Look for parasitized red blood cells.
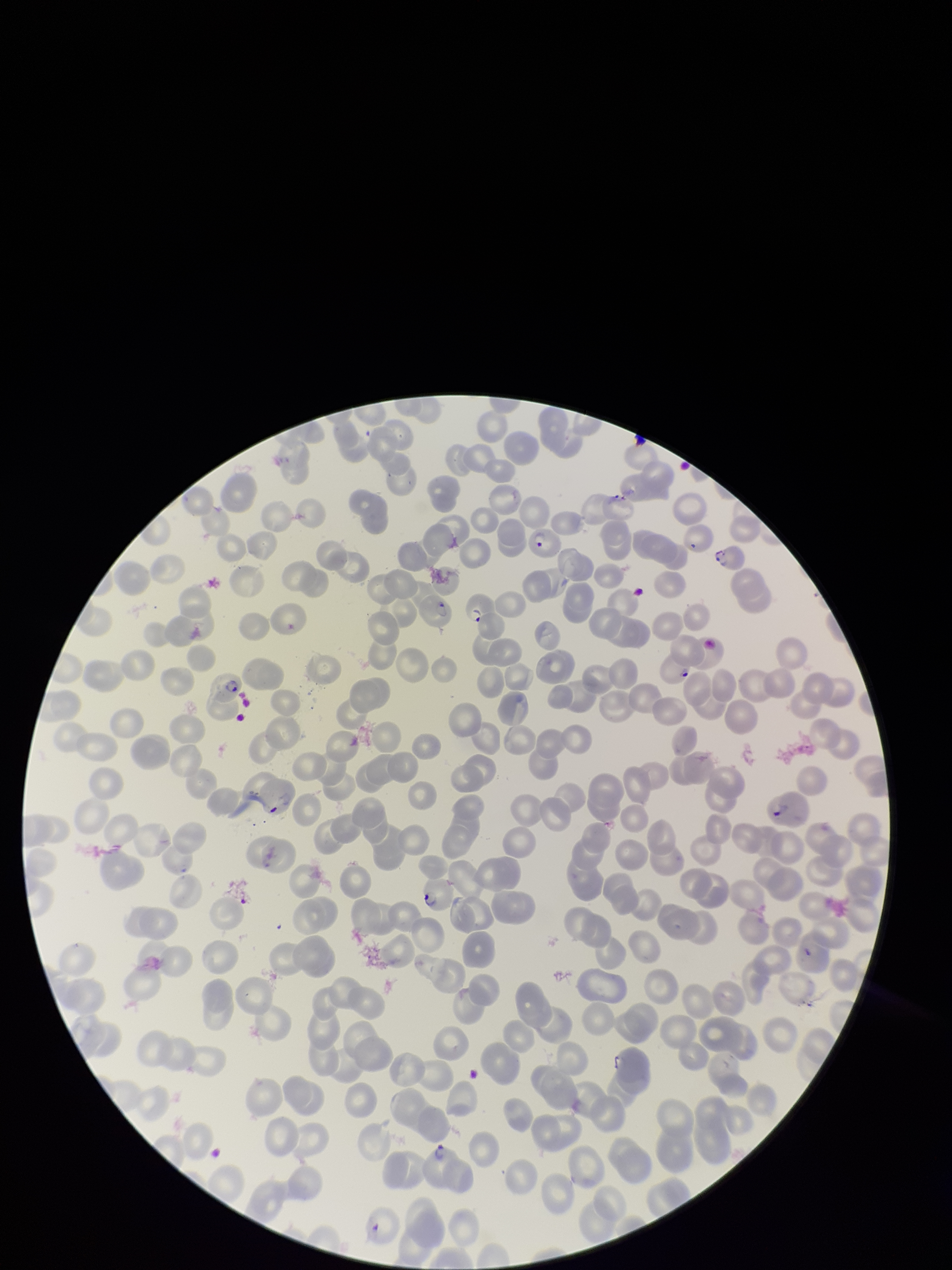

Identified.

Image is 952×1270 pixels. Species reported for this patient: Plasmodium falciparum. Patient malaria status: infected. Red blood cell count: 226. Giemsa stain. Single field of view. Preparation: thin blood smear. Parasitized red blood cell count: 10. Photographed through the microscope eyepiece with a smartphone camera.